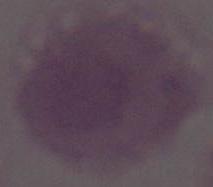
Summary:
  - Identification: erythrocyte
  - Modality: micrograph
  - Magnification: 1000x